Outline platelets.
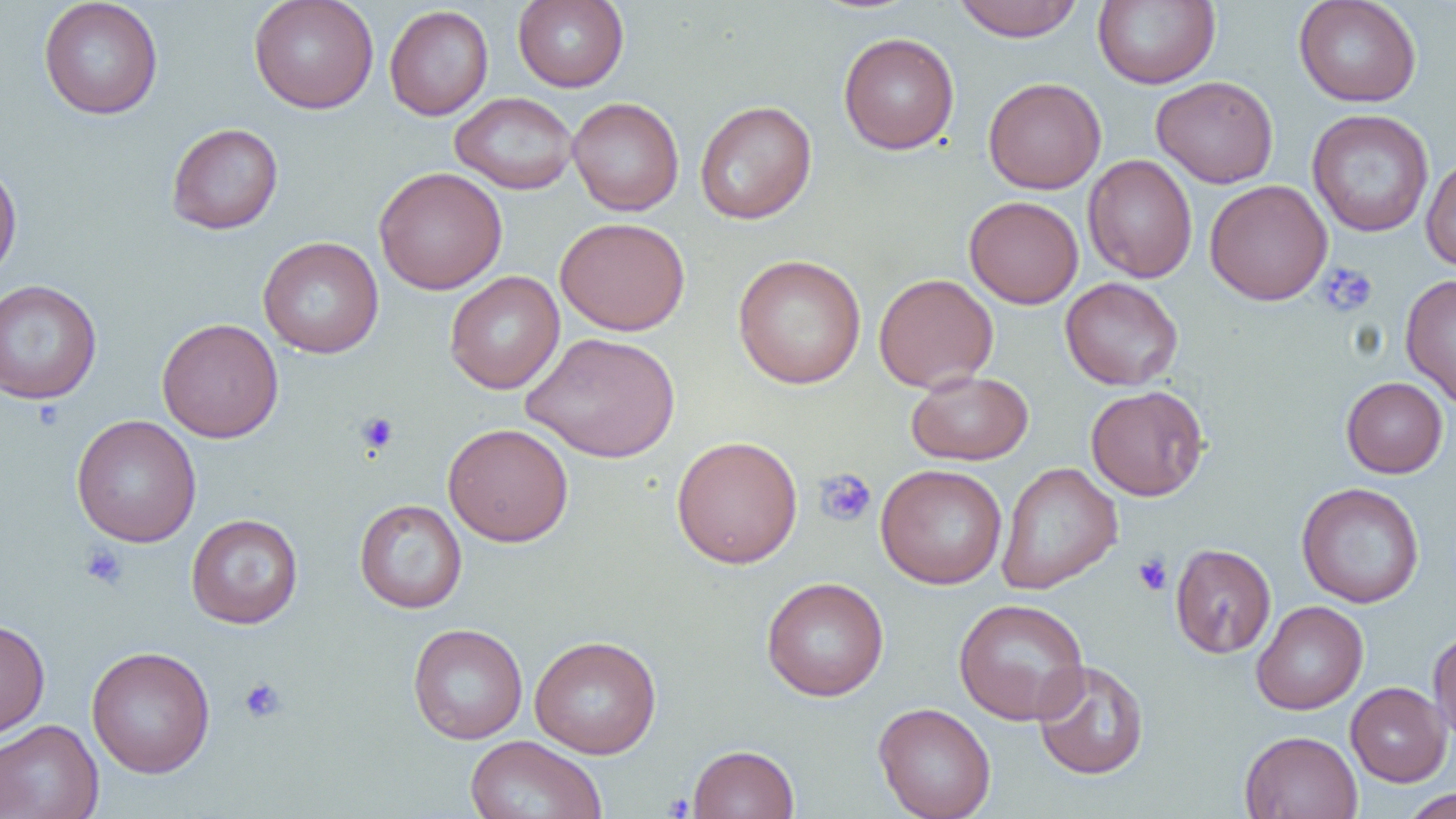
Approximate bounding boxes as (x1, y1, x2, y2) in pixels.
Platelets: (1317, 263, 1377, 316), (356, 412, 399, 454), (814, 468, 876, 527), (79, 542, 129, 590), (1133, 554, 1172, 595), (239, 677, 287, 724).

Summary:
  - Uninfected red blood cell locations: (38, 0, 164, 119), (248, 0, 379, 114), (512, 0, 629, 92), (952, 0, 1084, 42), (1092, 0, 1220, 89), (1293, 0, 1422, 107), (384, 5, 493, 120), (838, 32, 960, 155), (1151, 75, 1279, 188), (982, 77, 1106, 194), (450, 91, 578, 194), (567, 97, 684, 216), (694, 100, 817, 224), (1306, 109, 1435, 237), (166, 123, 284, 235), (1083, 155, 1198, 283), (1420, 155, 1456, 272), (0, 157, 22, 284), (373, 166, 507, 295), (1204, 179, 1332, 305), (963, 195, 1084, 309), (555, 215, 690, 336), (258, 236, 384, 358), (732, 254, 866, 389), (444, 271, 565, 394), (873, 272, 999, 392), (1400, 274, 1456, 409), (1060, 277, 1184, 391), (0, 279, 102, 405), (157, 317, 284, 443), (521, 331, 680, 463), (906, 370, 1034, 465), (1341, 377, 1449, 478), (1085, 385, 1209, 501), (71, 414, 201, 547), (443, 422, 574, 546), (671, 435, 803, 569), (996, 462, 1123, 595), (875, 464, 1007, 589), (1296, 482, 1424, 608), (354, 498, 467, 613), (186, 514, 303, 629), (1170, 543, 1276, 659), (761, 576, 889, 701), (953, 597, 1091, 725), (1251, 600, 1368, 715), (0, 618, 50, 738), (407, 623, 528, 744), (1428, 627, 1456, 744), (529, 635, 662, 759), (86, 645, 215, 778), (1032, 660, 1150, 780), (1346, 682, 1451, 786), (873, 702, 997, 819), (0, 719, 104, 819), (1240, 730, 1362, 819), (464, 735, 608, 819), (688, 744, 799, 818), (1399, 788, 1455, 818)
  - Slide-level diagnosis: negative for blood parasites
  - Modality: light microscopy
  - Magnification: 1000x
  - Preparation: thin blood smear
  - Field of view: one of a larger specimen
  - Image size: 1456×819 pixels